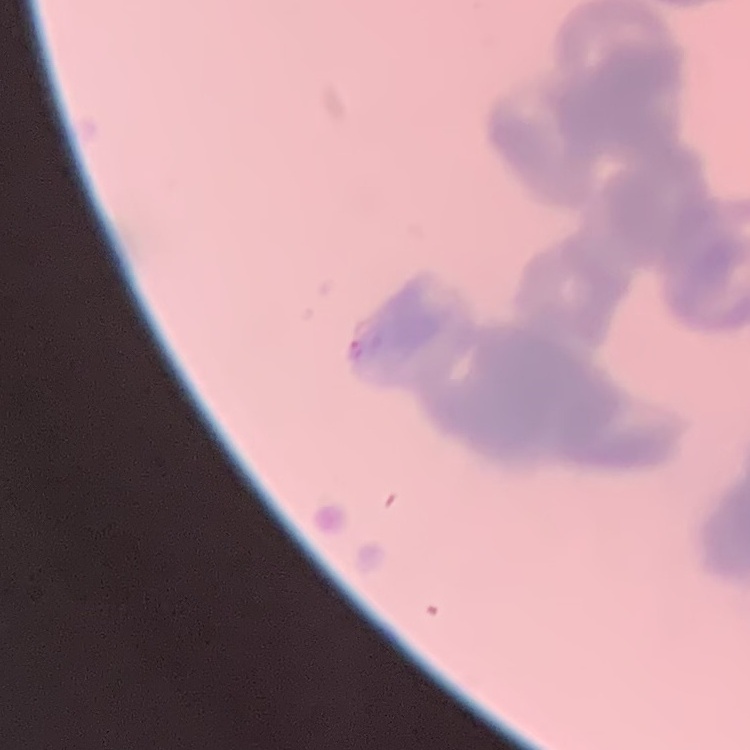 The erythrocytes exhibit rouleaux formation. Thin blood smear. Stained with either Field's or Giemsa. Square crop of a larger photomicrograph.